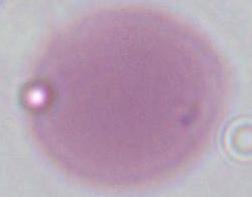 Micrograph. An erythrocyte is shown. Captured at 1000x magnification.